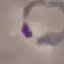

Summary:
  - Result: malaria parasites identified
  - Image type: automatically extracted cell patch, resized to 64 × 64 pixels
  - Stain: Giemsa
  - Capture: smartphone through the microscope eyepiece
  - Preparation: thin smear